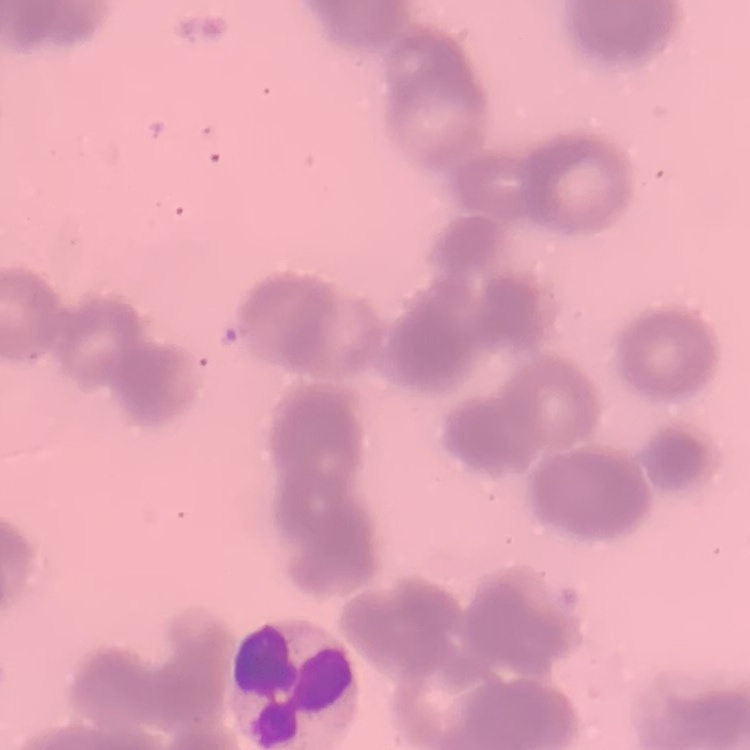
The erythrocytes show rouleaux formation. One tile cut from a larger photomicrograph. Field's or Giemsa stain. Thin peripheral smear.